Comment on the morphology of the erythrocytes.
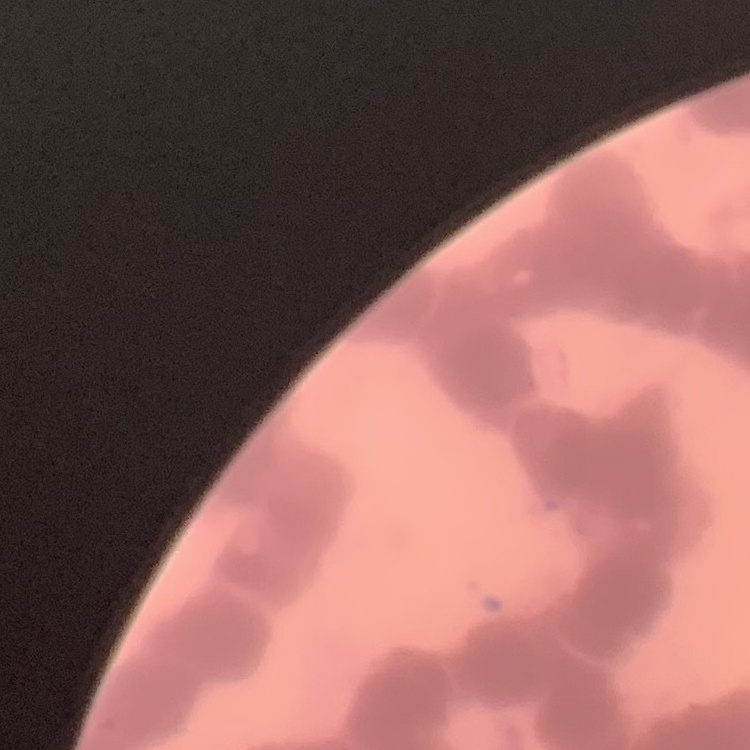

They show rouleaux formation.

Thin blood film. One tile cut from a larger photomicrograph. Stained with either Field's or Giemsa.